Assess this cell for malaria.
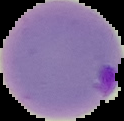

It is parasitized.

Summary:
  - Image size: 124×121 pixels
  - Image type: cell region segmented out of the field of view; surrounding area masked to black
  - Preparation: thin blood film